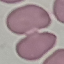

Malaria status: uninfected. Acquired by smartphone through the microscope eyepiece. Giemsa stain. Thin blood film. Cell patch, automatically extracted from a larger field of view and resized to 64 × 64 pixels.